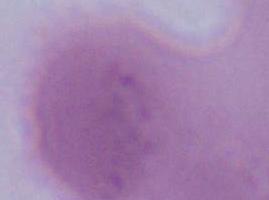

1000x magnification. Micrograph. A red blood cell is seen.